Report the malaria status of this cell.
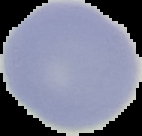

It is uninfected.

Summary:
  - Preparation: thin blood smear
  - Image type: segmented cell region with the area outside set to black
  - Image size: 142×136 pixels